Report the malaria status of this cell.
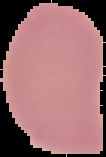
Uninfected.

preparation = thin blood smear
image size = 106×157 pixels
image type = cell region segmented out of the field of view; surrounding area masked to black